Assess the morphology of the erythrocytes.
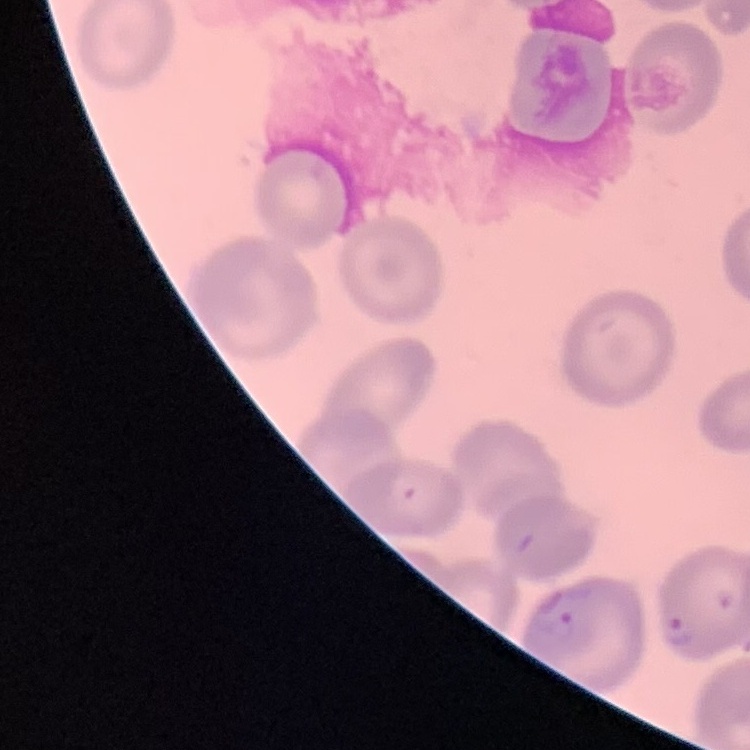

No rouleaux formation.

image type = one tile cut from a larger photomicrograph
preparation = thin blood smear
stain = Field's or Giemsa